Give the extent of all uninfected red blood cells.
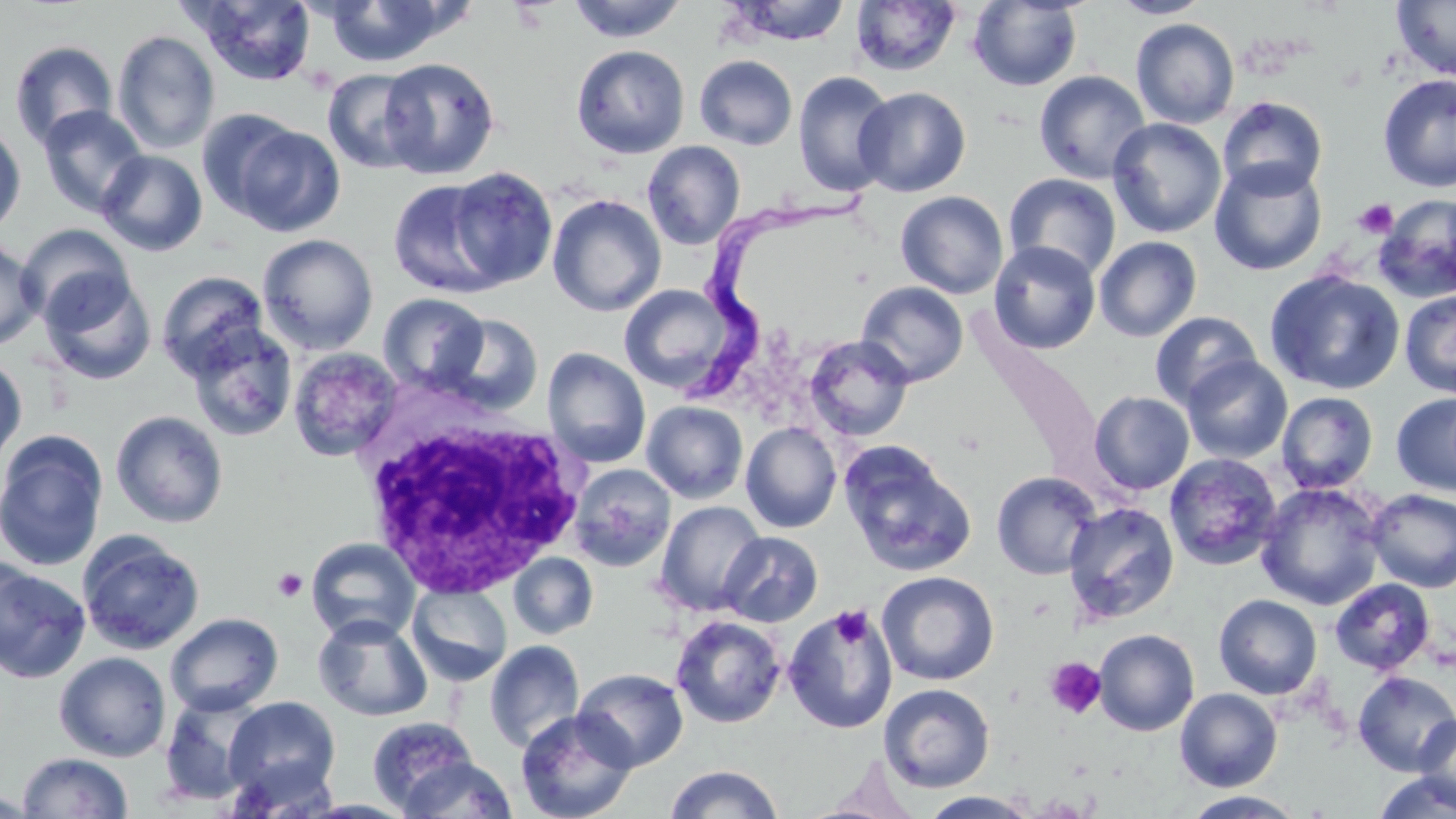
Approximate bounding boxes as [x1, y1, x2, y2] in pixels.
Uninfected red blood cells: [324, 0, 457, 67], [566, 0, 689, 43], [1108, 0, 1213, 18], [1391, 0, 1456, 82], [188, 1, 318, 85], [728, 1, 850, 45], [849, 1, 962, 77], [968, 1, 1083, 91], [1131, 18, 1239, 128], [112, 29, 221, 155], [9, 40, 118, 149], [571, 44, 690, 158], [694, 55, 797, 150], [378, 57, 500, 179], [322, 69, 426, 174], [1034, 69, 1151, 184], [793, 71, 897, 196], [1378, 74, 1456, 192], [854, 86, 971, 197], [1217, 96, 1328, 200], [37, 105, 149, 218], [196, 108, 305, 221], [1107, 117, 1227, 239], [0, 122, 26, 236], [227, 122, 346, 236], [642, 140, 746, 250], [96, 149, 207, 256], [1209, 159, 1327, 276], [445, 167, 558, 289], [1004, 173, 1121, 281], [388, 178, 509, 298], [896, 190, 1009, 299], [547, 194, 667, 317], [1375, 195, 1456, 303], [16, 223, 136, 327], [258, 234, 378, 355], [0, 236, 44, 351], [1094, 236, 1202, 342], [988, 241, 1101, 354], [1264, 268, 1406, 395], [39, 270, 157, 385], [155, 270, 269, 378], [856, 281, 969, 387], [619, 284, 740, 394], [1399, 290, 1456, 398], [378, 293, 490, 393], [1150, 311, 1262, 410], [438, 314, 544, 414], [184, 322, 298, 441], [805, 335, 914, 441], [287, 347, 403, 462], [543, 348, 650, 468], [0, 354, 27, 469], [1181, 356, 1293, 465], [1089, 391, 1194, 494], [1276, 391, 1379, 493], [1391, 392, 1456, 497], [641, 400, 749, 503], [110, 410, 229, 528], [741, 422, 842, 533], [0, 431, 109, 572], [840, 442, 977, 578], [1164, 453, 1281, 571], [569, 463, 676, 572], [991, 471, 1102, 580], [1255, 482, 1387, 610], [1366, 488, 1456, 592], [655, 500, 767, 616], [1063, 502, 1180, 626], [76, 530, 206, 655], [717, 531, 823, 627], [305, 538, 421, 644], [0, 552, 34, 659], [509, 553, 598, 639], [0, 568, 91, 683], [877, 571, 999, 685], [1330, 578, 1434, 675], [407, 583, 513, 685], [1213, 594, 1322, 699], [783, 605, 898, 734], [165, 612, 284, 716], [313, 614, 432, 722], [670, 615, 786, 728], [1093, 629, 1200, 735], [484, 639, 585, 752], [54, 651, 172, 762], [574, 668, 689, 771], [1352, 670, 1456, 776], [879, 683, 995, 792], [1175, 689, 1283, 791], [157, 693, 269, 806], [223, 697, 342, 804], [515, 708, 639, 819], [1412, 713, 1456, 813], [367, 715, 480, 815], [17, 752, 134, 817], [399, 756, 517, 818], [664, 764, 784, 819], [1372, 772, 1455, 819], [919, 790, 1041, 818], [1181, 791, 1306, 818].

slide-level diagnosis = Trypanosoma brucei
field of view = single
image size = 1456×819 pixels
modality = light microscopy
Trypanosoma brucei locations = approximate bounding boxes as [x1, y1, x2, y2] in pixels: [684, 183, 886, 396]
platelet locations = approximate bounding boxes as [x1, y1, x2, y2] in pixels: [1353, 198, 1398, 239], [272, 569, 308, 602], [830, 605, 874, 650], [1044, 657, 1107, 719]
magnification = 1000x
preparation = thin blood film
white blood cell locations = approximate bounding boxes as [x1, y1, x2, y2] in pixels: [349, 403, 597, 600]
stain = May-Grünwald-Giemsa